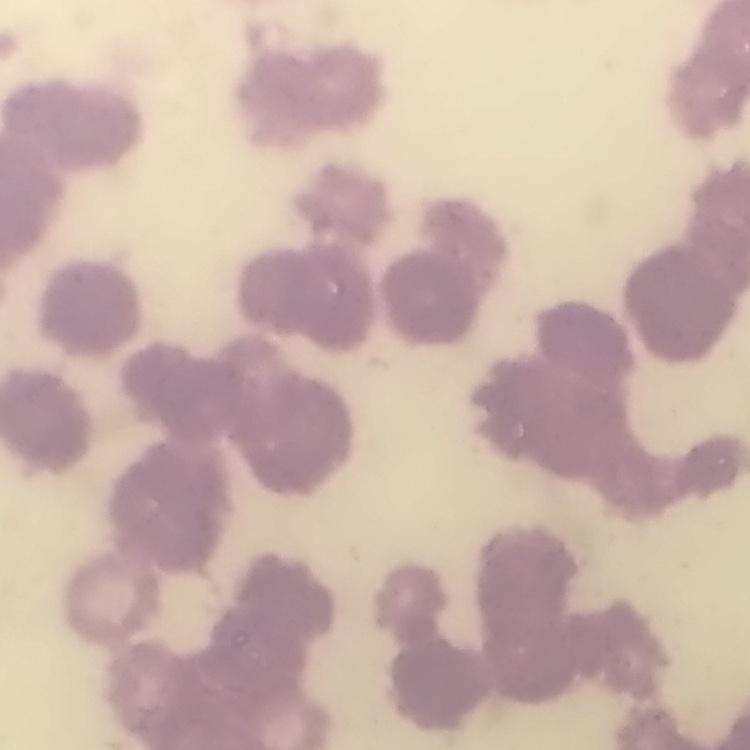

Summary:
  - Erythrocyte morphology: rouleaux formation
  - Preparation: thin blood film
  - Stain: Field's or Giemsa
  - Image type: one tile cut from a larger photomicrograph